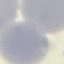
Summary:
  - Result: negative for malaria parasites
  - Capture: smartphone camera at the microscope eyepiece
  - Image type: cell patch, automatically extracted from a larger field of view and resized to 64 × 64 pixels
  - Preparation: thin blood smear
  - Stain: Giemsa